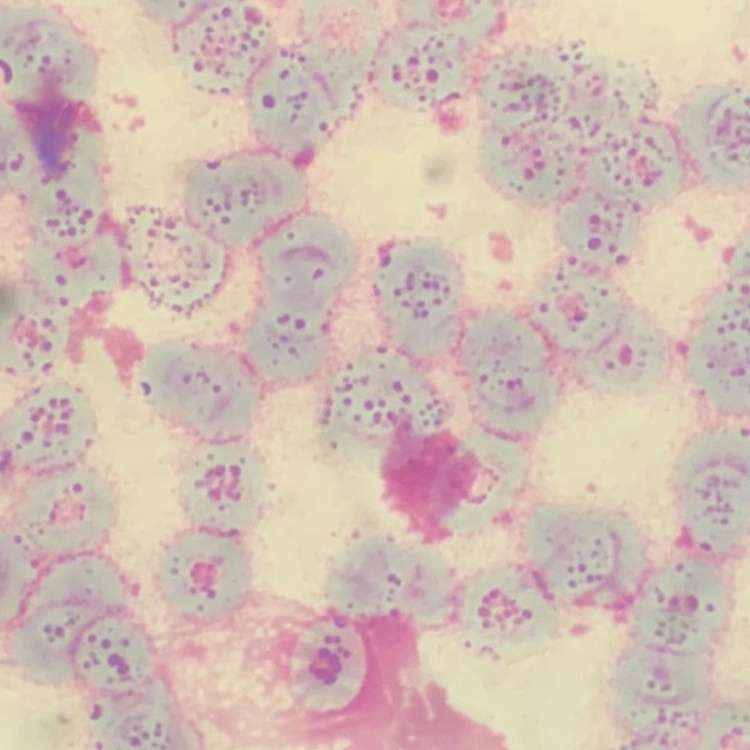

red_blood_cell_morphology: rouleaux formation
stain: Field's or Giemsa
preparation: thin blood smear
image_type: one tile cut from a larger photomicrograph